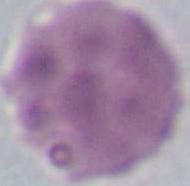
Summary:
  - Modality: photomicrograph
  - Identification: erythrocyte
  - Magnification: 1000x